Locate every malaria parasite.
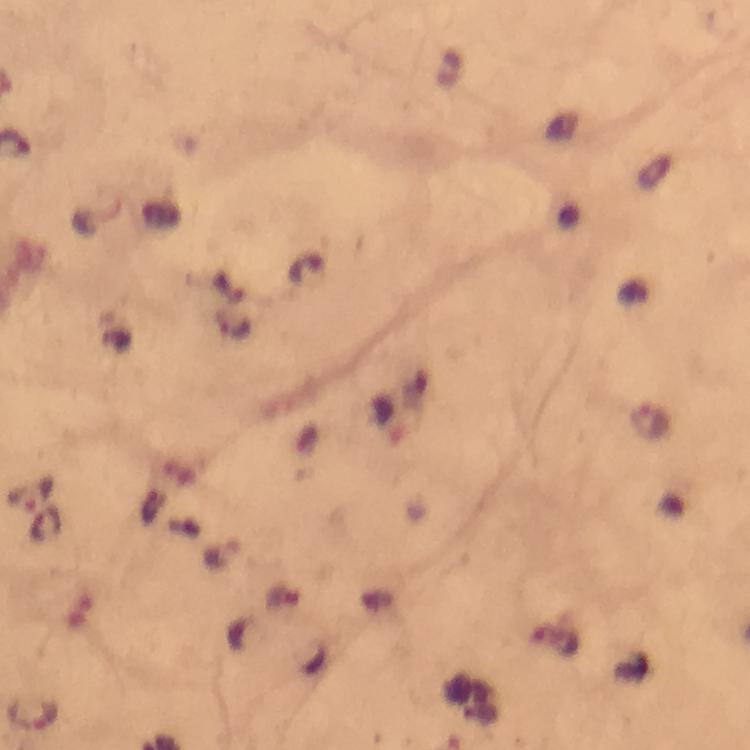

Approximate object centers, in pixels from the top-left corner.
Malaria parasites: (x=232, y=326), (x=32, y=493), (x=45, y=525), (x=34, y=713).

At 100x magnification. Photographed through the microscope with a smartphone camera. Giemsa stain. From a malaria diagnostic workup. Image is 750×750 pixels. Immersion oil applied. Cropped region of a single field of view. Thick blood smear.